Outline each uninfected red blood cell.
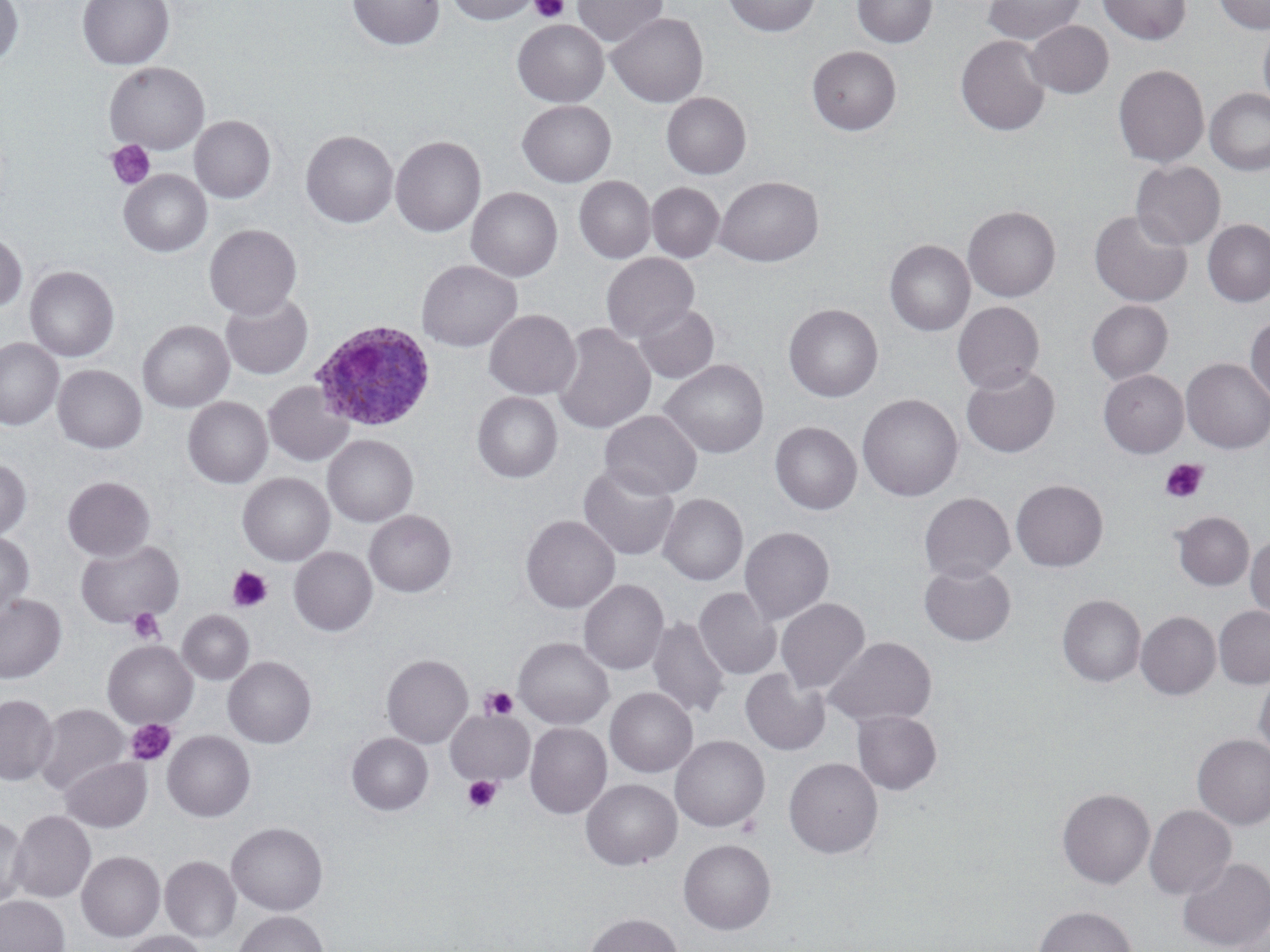

Approximate bounding boxes as named x1/y1/x2/y2 corners in pixels.
Uninfected red blood cells: (x1=0, y1=0, x2=24, y2=69), (x1=77, y1=0, x2=174, y2=69), (x1=346, y1=0, x2=445, y2=51), (x1=447, y1=0, x2=540, y2=25), (x1=572, y1=0, x2=668, y2=49), (x1=723, y1=0, x2=821, y2=37), (x1=852, y1=0, x2=938, y2=48), (x1=983, y1=0, x2=1085, y2=45), (x1=1098, y1=0, x2=1191, y2=44), (x1=1213, y1=0, x2=1270, y2=34), (x1=606, y1=12, x2=708, y2=107), (x1=512, y1=19, x2=609, y2=107), (x1=1024, y1=20, x2=1113, y2=98), (x1=1258, y1=22, x2=1270, y2=115), (x1=955, y1=35, x2=1051, y2=136), (x1=807, y1=46, x2=902, y2=135), (x1=104, y1=62, x2=209, y2=154), (x1=1113, y1=64, x2=1208, y2=168), (x1=1205, y1=88, x2=1270, y2=176), (x1=661, y1=92, x2=751, y2=179), (x1=517, y1=100, x2=616, y2=187), (x1=190, y1=116, x2=275, y2=203), (x1=301, y1=130, x2=398, y2=228), (x1=390, y1=135, x2=487, y2=237), (x1=1131, y1=160, x2=1226, y2=250), (x1=119, y1=170, x2=212, y2=257), (x1=574, y1=176, x2=656, y2=264), (x1=715, y1=176, x2=823, y2=267), (x1=647, y1=183, x2=724, y2=262), (x1=466, y1=187, x2=563, y2=282), (x1=963, y1=205, x2=1061, y2=302), (x1=1089, y1=209, x2=1193, y2=307), (x1=1202, y1=219, x2=1270, y2=307), (x1=204, y1=224, x2=302, y2=320), (x1=0, y1=231, x2=28, y2=313), (x1=885, y1=240, x2=974, y2=336), (x1=601, y1=253, x2=699, y2=343), (x1=417, y1=260, x2=523, y2=352), (x1=25, y1=266, x2=119, y2=362), (x1=221, y1=293, x2=314, y2=380), (x1=1087, y1=300, x2=1173, y2=384), (x1=952, y1=301, x2=1044, y2=394), (x1=633, y1=303, x2=719, y2=383), (x1=783, y1=303, x2=883, y2=402), (x1=484, y1=309, x2=581, y2=399), (x1=1245, y1=316, x2=1270, y2=404), (x1=137, y1=320, x2=234, y2=412), (x1=551, y1=322, x2=656, y2=434), (x1=0, y1=338, x2=63, y2=431), (x1=1181, y1=358, x2=1270, y2=453), (x1=660, y1=360, x2=768, y2=459), (x1=53, y1=365, x2=147, y2=454), (x1=961, y1=365, x2=1060, y2=458), (x1=1098, y1=370, x2=1188, y2=458), (x1=263, y1=380, x2=354, y2=466), (x1=472, y1=392, x2=563, y2=483), (x1=857, y1=394, x2=963, y2=502), (x1=183, y1=397, x2=273, y2=488), (x1=599, y1=410, x2=702, y2=500), (x1=769, y1=415, x2=961, y2=508), (x1=770, y1=422, x2=861, y2=514), (x1=323, y1=435, x2=418, y2=527), (x1=0, y1=459, x2=32, y2=540), (x1=578, y1=462, x2=680, y2=561), (x1=237, y1=473, x2=335, y2=566), (x1=62, y1=476, x2=155, y2=561), (x1=1011, y1=479, x2=1108, y2=572), (x1=658, y1=493, x2=748, y2=586), (x1=919, y1=493, x2=1015, y2=583), (x1=364, y1=510, x2=456, y2=597), (x1=1171, y1=511, x2=1254, y2=590), (x1=520, y1=515, x2=620, y2=613), (x1=739, y1=526, x2=835, y2=625), (x1=0, y1=532, x2=34, y2=614), (x1=1246, y1=535, x2=1270, y2=621), (x1=75, y1=540, x2=184, y2=627), (x1=289, y1=547, x2=378, y2=636), (x1=919, y1=562, x2=1017, y2=646), (x1=578, y1=579, x2=669, y2=675), (x1=694, y1=587, x2=781, y2=679), (x1=0, y1=594, x2=66, y2=683), (x1=1057, y1=594, x2=1146, y2=687), (x1=776, y1=598, x2=870, y2=694), (x1=1214, y1=605, x2=1270, y2=688), (x1=177, y1=610, x2=254, y2=685), (x1=1136, y1=611, x2=1221, y2=700), (x1=647, y1=617, x2=731, y2=720), (x1=825, y1=636, x2=937, y2=728), (x1=514, y1=638, x2=613, y2=728), (x1=102, y1=640, x2=198, y2=728), (x1=381, y1=654, x2=473, y2=748), (x1=223, y1=656, x2=316, y2=748), (x1=740, y1=668, x2=830, y2=756), (x1=1254, y1=671, x2=1270, y2=762), (x1=605, y1=688, x2=698, y2=777), (x1=0, y1=694, x2=59, y2=785), (x1=34, y1=703, x2=129, y2=797), (x1=446, y1=709, x2=535, y2=786), (x1=851, y1=710, x2=942, y2=795), (x1=525, y1=722, x2=612, y2=819), (x1=162, y1=730, x2=255, y2=822), (x1=346, y1=732, x2=433, y2=815), (x1=1193, y1=734, x2=1270, y2=830), (x1=670, y1=735, x2=769, y2=831), (x1=59, y1=756, x2=152, y2=832), (x1=784, y1=757, x2=883, y2=858), (x1=581, y1=778, x2=682, y2=870), (x1=1057, y1=787, x2=1155, y2=888), (x1=1144, y1=804, x2=1236, y2=900), (x1=9, y1=810, x2=96, y2=903), (x1=0, y1=815, x2=30, y2=908), (x1=226, y1=822, x2=328, y2=915), (x1=678, y1=838, x2=776, y2=934), (x1=77, y1=851, x2=165, y2=941), (x1=160, y1=856, x2=241, y2=942), (x1=1178, y1=856, x2=1270, y2=951), (x1=0, y1=895, x2=70, y2=952), (x1=1033, y1=905, x2=1138, y2=952), (x1=1227, y1=908, x2=1270, y2=952), (x1=234, y1=910, x2=329, y2=952), (x1=585, y1=912, x2=682, y2=952), (x1=118, y1=930, x2=209, y2=952).

Plasmodium ovale-infected red blood cell locations: (x1=311, y1=320, x2=437, y2=434). Platelet locations: (x1=530, y1=0, x2=570, y2=23), (x1=106, y1=140, x2=156, y2=190), (x1=1160, y1=458, x2=1208, y2=504), (x1=227, y1=566, x2=272, y2=612), (x1=127, y1=608, x2=164, y2=644), (x1=480, y1=687, x2=518, y2=721), (x1=126, y1=718, x2=175, y2=765), (x1=462, y1=775, x2=502, y2=814). Slide-level diagnosis: Plasmodium ovale. Image is 1270×952 pixels. May-Grünwald-Giemsa-stained preparation. Thin blood smear. Single field of view. Light microscopy. 1000x magnification.